Assess this cell for malaria.
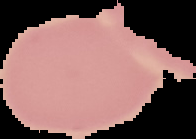
It is uninfected.

preparation: thin blood film
image_type: segmented cell region on a black background
image_size: 196×139 pixels